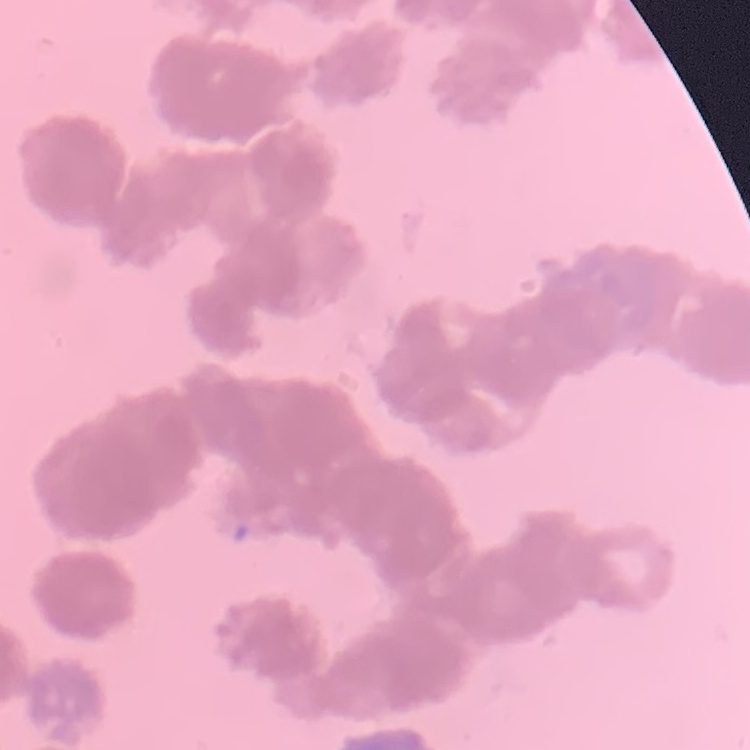

Summary:
  - Red blood cell morphology: rouleaux formation
  - Preparation: thin peripheral smear
  - Stain: Field's or Giemsa
  - Image type: one tile cut from a larger photomicrograph